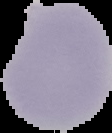
Summary:
  - Image size: 112×133 pixels
  - Malaria status: uninfected
  - Preparation: thin blood smear
  - Image type: segmented cell region with the area outside set to black